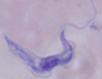 A trypanosome is shown. Photomicrograph. 1000x magnification.